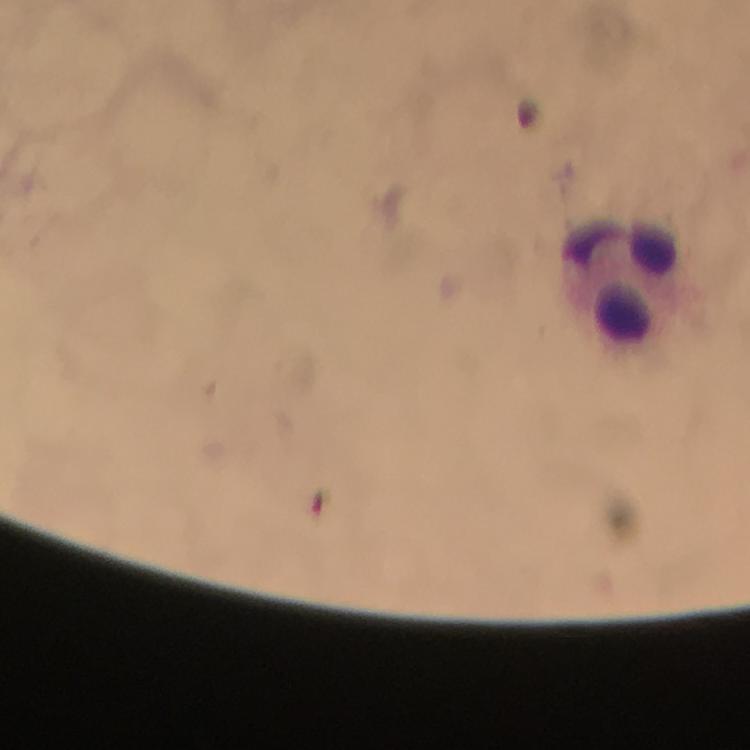

Approximate object centers, in pixels from the top-left corner. Leukocyte locations: (x=621, y=285). 100x magnification. Immersion oil applied. From a malaria diagnostic workup. Photographed with a smartphone mounted on the microscope. Cropped region of a single field of view. Giemsa stain. Malaria parasites: none detected. Thick blood smear. Image is 750×750 pixels.